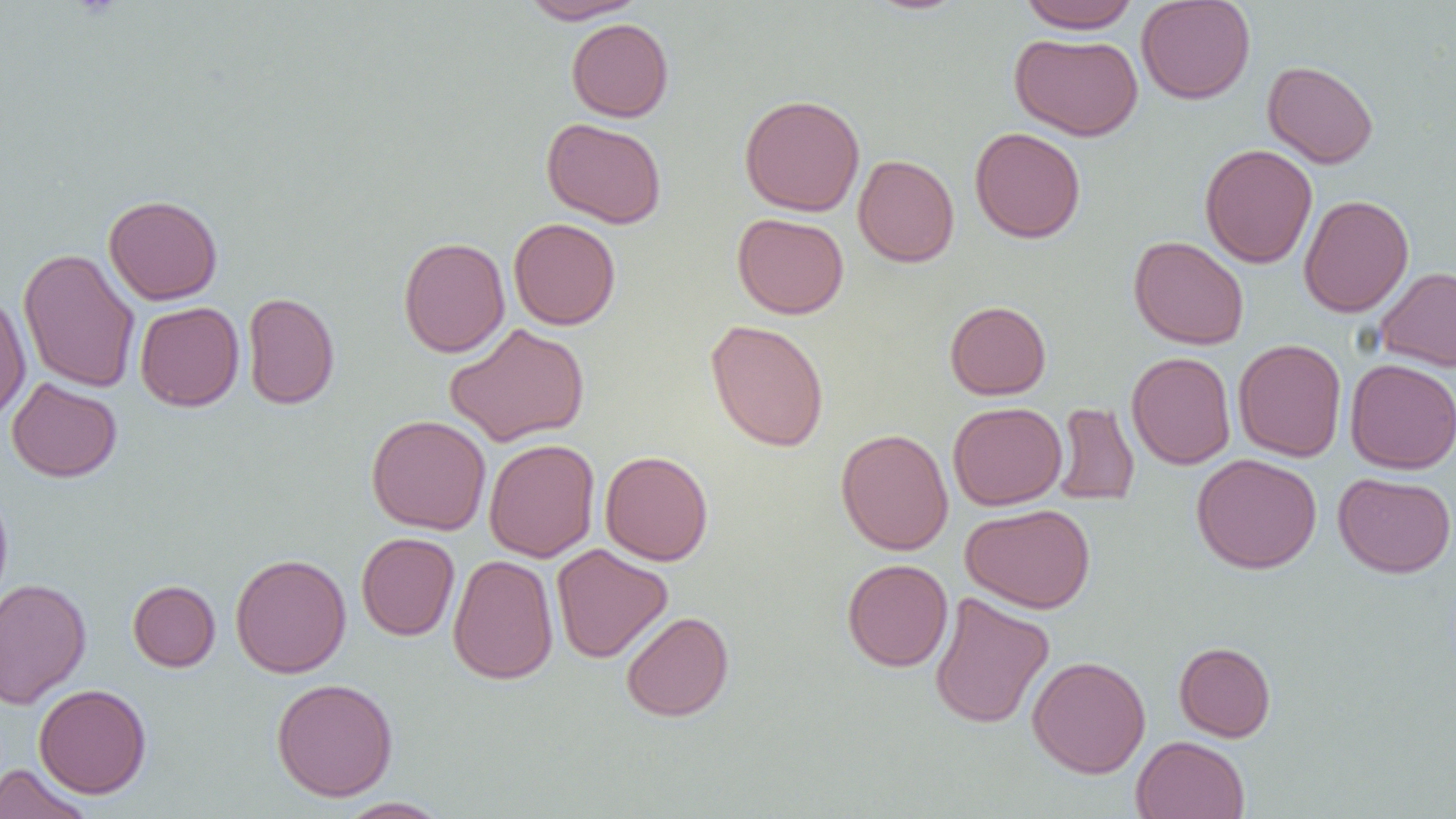
{
  "slide_level_diagnosis": "negative for blood parasites",
  "magnification": "1000x",
  "image_size": "1456×819 pixels",
  "preparation": "thin blood film",
  "modality": "optical microscopy",
  "field_of_view": "single",
  "uninfected_red_blood_cell_locations": "approximate bounding boxes as (x1,y1)-(x2,y2) corner pairs in pixels: (518,0)-(646,24), (1018,0)-(1139,33), (1136,0)-(1256,104), (566,18)-(674,122), (1010,32)-(1144,141), (1262,60)-(1379,169), (739,94)-(865,216), (541,117)-(667,228), (970,126)-(1086,243), (1200,143)-(1318,268), (853,154)-(959,268), (103,194)-(223,305), (1299,194)-(1414,317), (732,213)-(849,319), (508,217)-(621,330), (1128,235)-(1249,350), (398,237)-(510,358), (18,247)-(140,394), (1374,266)-(1456,372), (243,292)-(340,409), (0,293)-(31,423), (944,300)-(1051,400), (135,301)-(244,411), (705,319)-(830,452), (444,323)-(590,447), (1232,338)-(1347,461), (1127,352)-(1236,469), (1344,358)-(1456,474), (7,378)-(122,482), (1053,401)-(1140,506), (948,402)-(1067,510), (366,414)-(491,535), (836,428)-(953,556), (484,438)-(600,562), (599,450)-(714,566), (1191,453)-(1322,574), (1333,472)-(1456,578), (0,484)-(13,612), (961,504)-(1096,614), (356,532)-(460,640), (551,544)-(673,663), (230,553)-(351,678), (447,554)-(559,684), (842,558)-(953,671), (1,578)-(92,708), (127,579)-(220,672), (929,591)-(1054,729), (621,611)-(734,722), (1174,641)-(1276,742), (1027,656)-(1151,778), (271,677)-(398,801), (34,683)-(151,799), (1132,735)-(1250,819), (0,763)-(94,819), (335,797)-(450,818)"
}